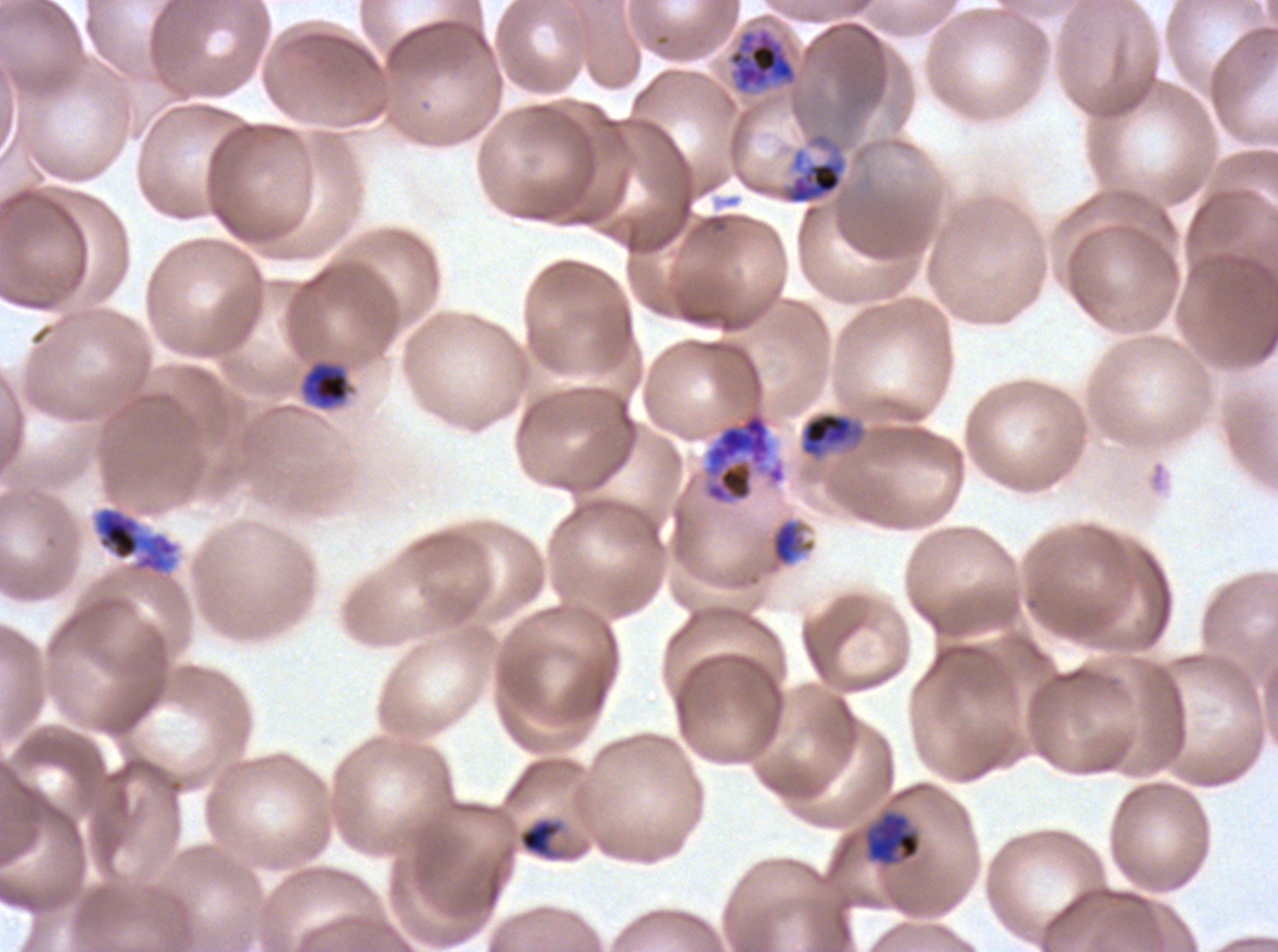

notation = approximate bounding boxes as [x1, y1, x2, y2] in pixels
late trophozoite locations = [779, 131, 848, 205]
early schizont locations = [728, 28, 797, 92], [92, 506, 180, 575]
late schizont locations = [703, 409, 787, 505]
mid trophozoite locations = [301, 361, 350, 409], [799, 411, 866, 460], [771, 519, 814, 566], [866, 812, 921, 865]
late-ring/early-trophozoite locations = [520, 819, 559, 856]
field of view = one sub-image of a larger composite
image size = 1278×952 pixels
preparation = thin blood film
specimen = Plasmodium falciparum from a patient in The Gambia, cultured ex vivo for 24 to 48 hours
life-cycle stages observed = late-ring/early-trophozoite, mid trophozoite, late trophozoite, early schizont, late schizont
stain = Giemsa